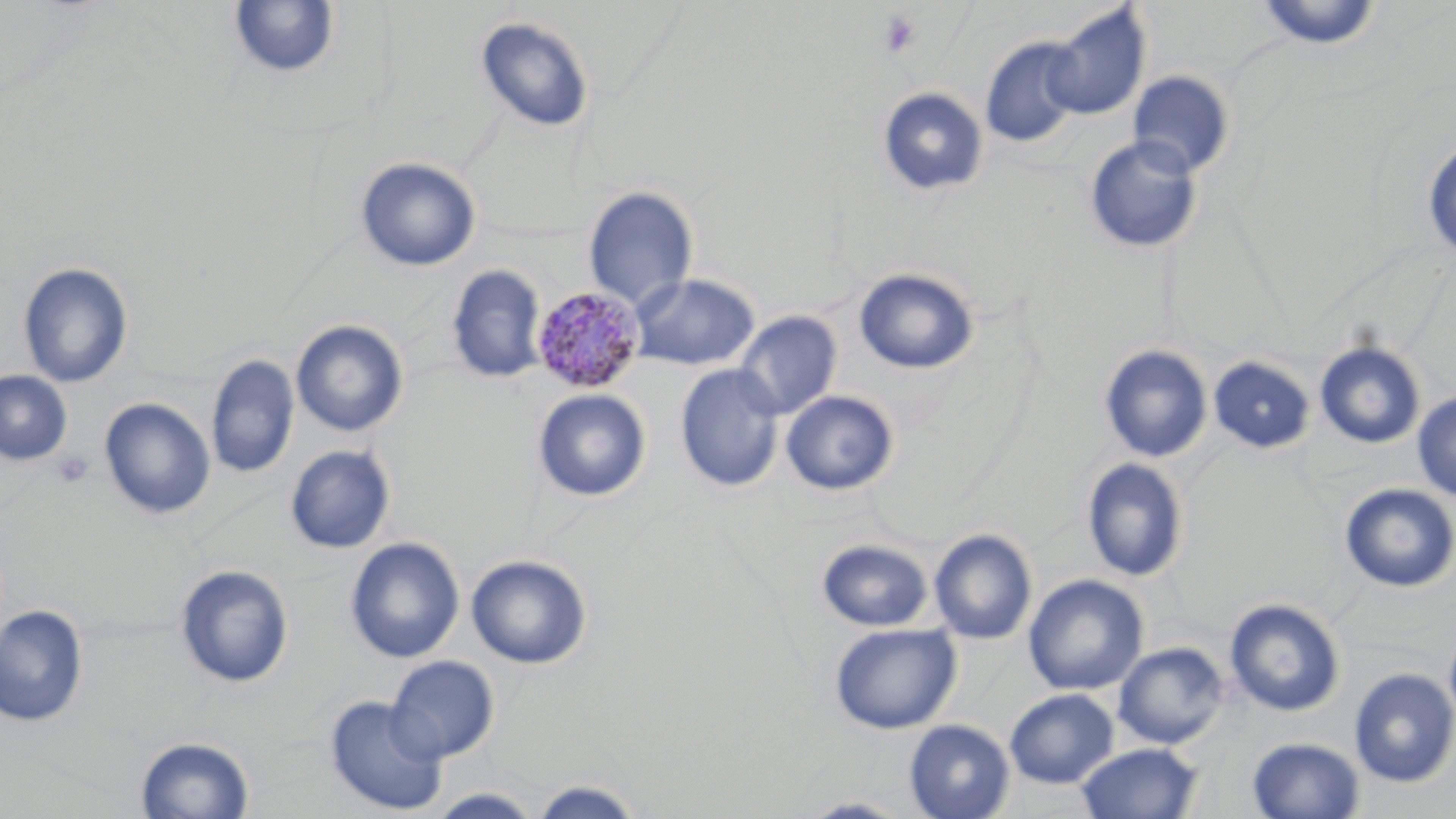

{
  "slide_level_diagnosis": "Plasmodium malariae",
  "preparation": "thin blood smear",
  "plasmodium_malariae_infected_red_blood_cell_locations": "approximate bounding boxes as [x1, y1, x2, y2] in pixels: [531, 285, 646, 396]",
  "magnification": "1000x",
  "uninfected_red_blood_cell_locations": "approximate bounding boxes as [x1, y1, x2, y2] in pixels: [228, 1, 339, 78], [1253, 1, 1382, 50], [1043, 5, 1150, 121], [475, 16, 595, 133], [980, 36, 1085, 148], [1128, 71, 1235, 177], [877, 87, 988, 196], [1083, 135, 1204, 253], [1422, 137, 1456, 262], [355, 157, 481, 271], [583, 186, 699, 310], [18, 262, 134, 387], [446, 264, 547, 383], [853, 267, 979, 374], [629, 273, 760, 371], [733, 311, 841, 420], [291, 319, 408, 437], [1315, 342, 1425, 449], [1099, 344, 1212, 462], [205, 354, 299, 479], [1208, 356, 1315, 453], [675, 364, 785, 492], [0, 370, 72, 465], [533, 388, 651, 502], [780, 390, 899, 496], [1412, 391, 1456, 502], [99, 398, 215, 519], [285, 445, 395, 553], [1082, 458, 1189, 582], [1339, 483, 1456, 593], [928, 528, 1037, 644], [345, 537, 465, 663], [817, 539, 932, 631], [465, 554, 592, 669], [175, 564, 294, 688], [1023, 574, 1149, 695], [1224, 599, 1345, 717], [0, 605, 88, 727], [829, 622, 961, 734], [1444, 622, 1456, 733], [1114, 642, 1229, 749], [386, 655, 500, 762], [1349, 667, 1456, 787], [1004, 688, 1119, 788], [324, 694, 449, 815], [904, 719, 1014, 819], [135, 736, 254, 818], [1247, 736, 1365, 818], [1076, 742, 1203, 819], [528, 779, 646, 819], [426, 788, 545, 818], [797, 797, 915, 818]",
  "platelet_locations": "approximate bounding boxes as [x1, y1, x2, y2] in pixels: [877, 10, 922, 58], [51, 450, 95, 489]",
  "modality": "light microscopy",
  "image_size": "1456×819 pixels",
  "field_of_view": "single",
  "stain": "May-Grünwald-Giemsa"
}